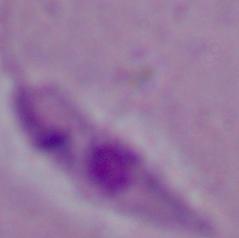
modality = micrograph
magnification = 1000x
identification = Leishmania